Give the preparation type.
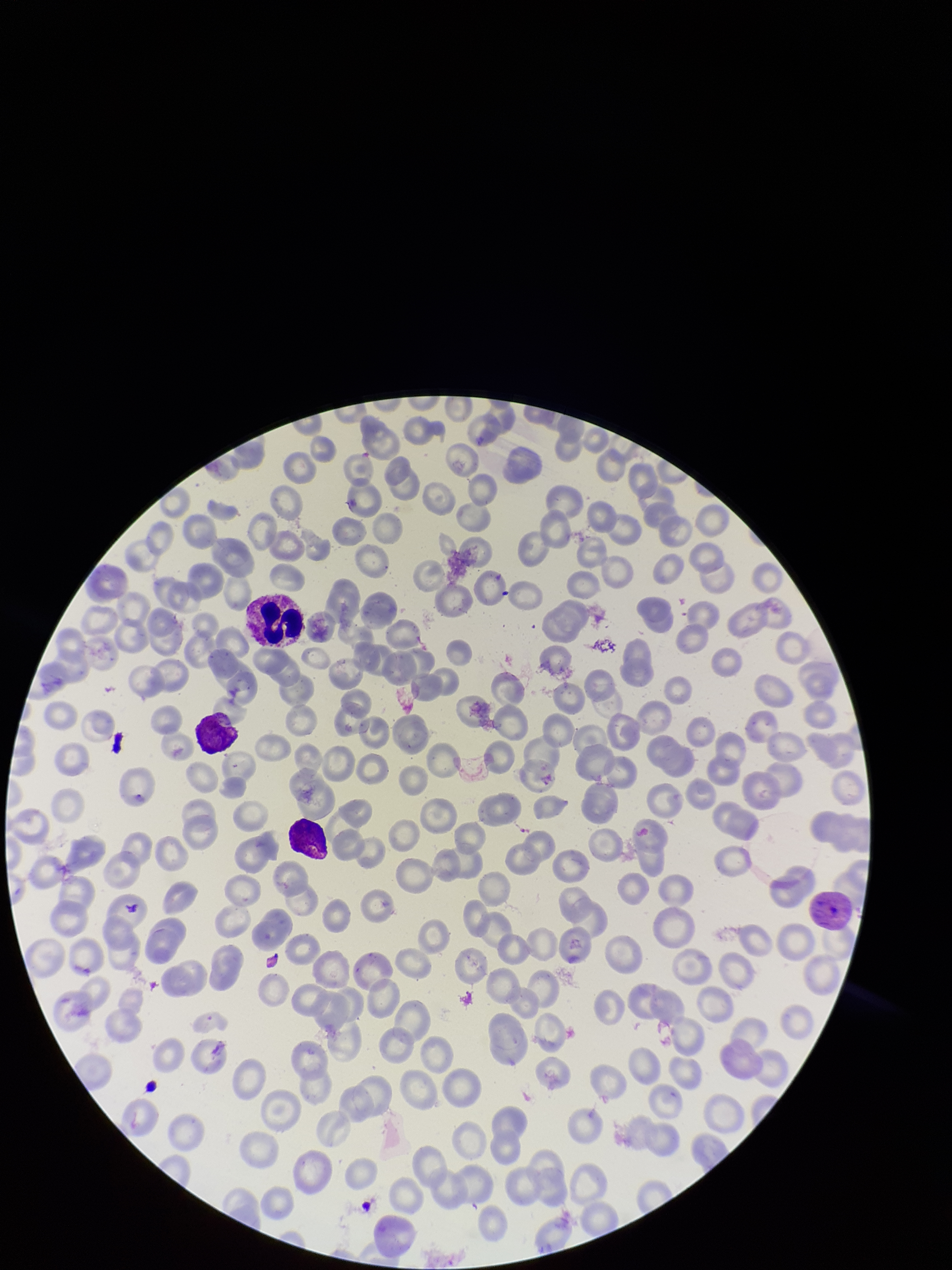

It is a thin blood smear.

Patient malaria status: infected. Species reported for this patient: Plasmodium vivax. Photographed through the microscope eyepiece with a smartphone camera. Stained with Giemsa. One field from this slide. Parasitized red blood cell count: 1. Parasitized red blood cells: detected. Red blood cell count: 185. Image is 952×1270 pixels.